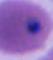 400x or 1000x magnification. Photomicrograph. A Plasmodium parasite is shown.